Assess the morphology of the red blood cells.
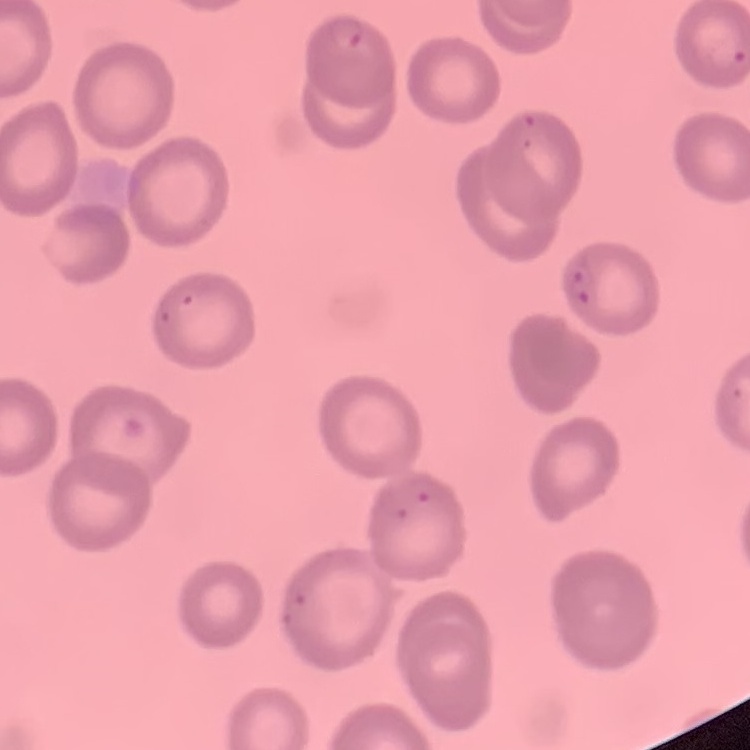

No rouleaux formation.

stain = Field's or Giemsa
image type = one tile cut from a larger photomicrograph
preparation = thin peripheral smear